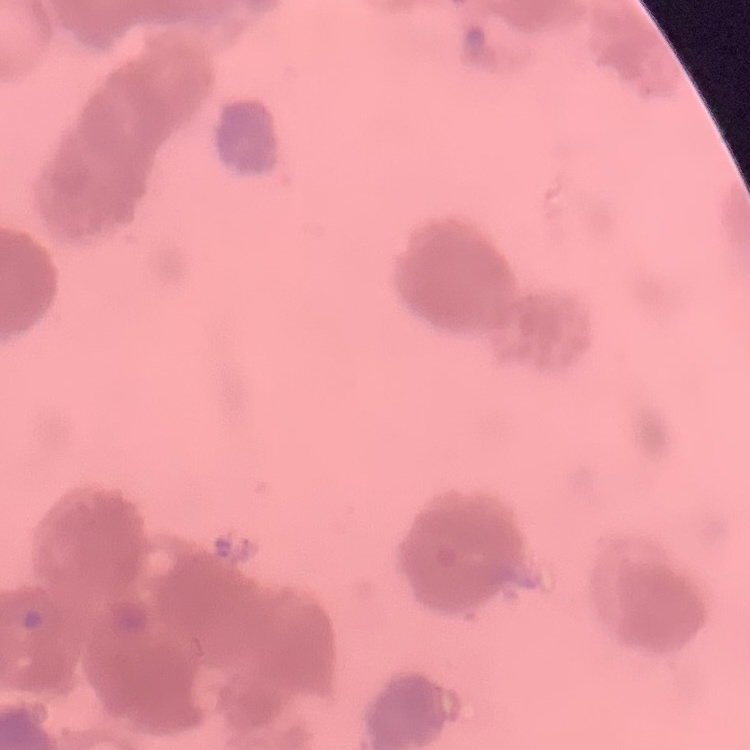 The erythrocytes exhibit rouleaux formation. Field's or Giemsa stain. Square crop of a larger photomicrograph. Thin blood film.